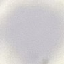
Result: no malaria parasites detected. Automatically extracted cell patch, resized to 64 × 64 pixels. Giemsa stain. Thin blood film. Acquired by smartphone through the microscope eyepiece.